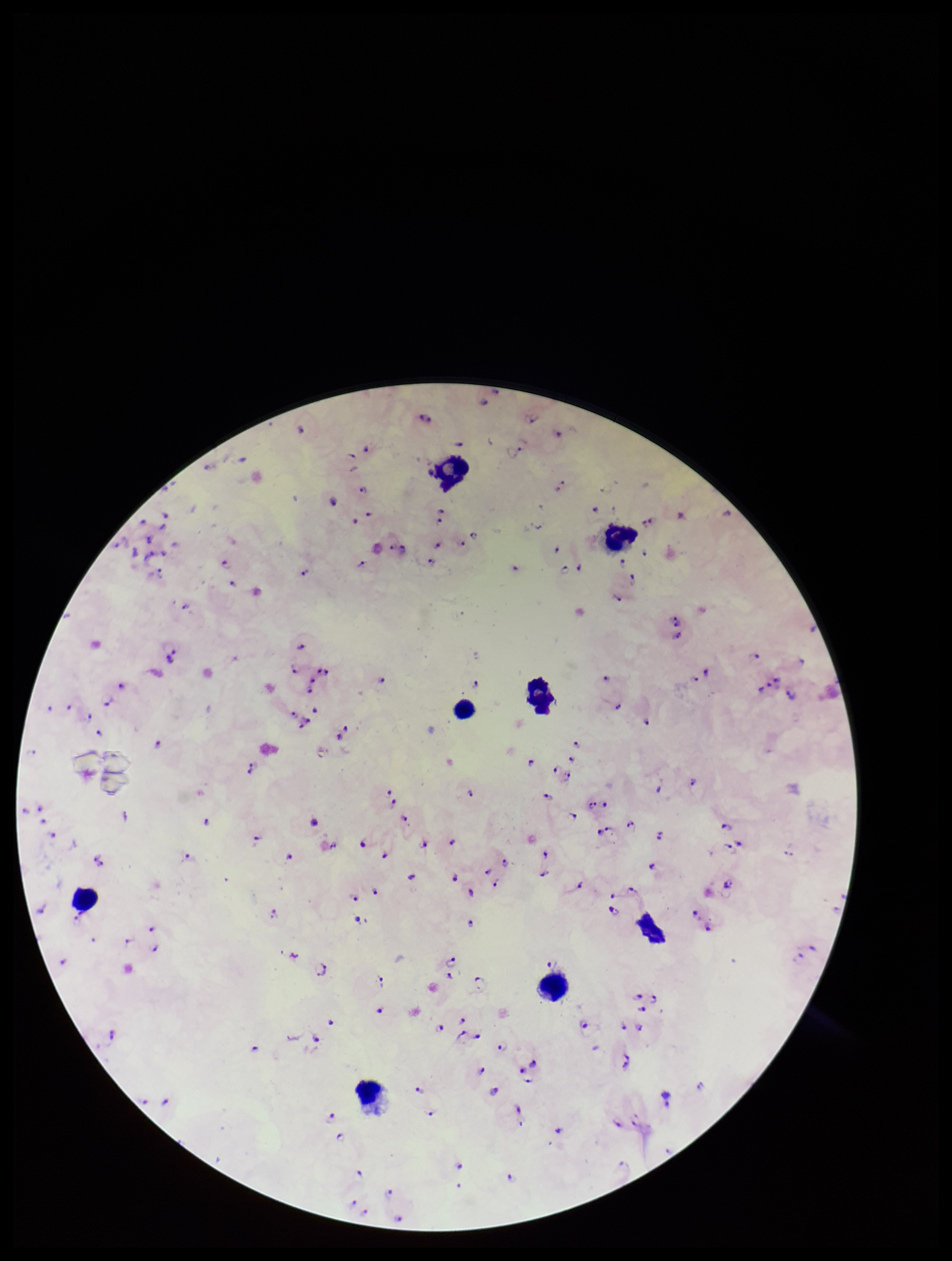 Image is 952×1261 pixels. Leukocyte count: 8. Plasmodium parasites: seen. Species reported for this patient: Plasmodium falciparum. Preparation: thick blood smear. Parasite count: 121. Single field of view. Patient malaria status: infected. Stained with Giemsa. Smartphone photograph taken through the eyepiece of a microscope.